Assess this cell for malaria.
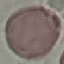
It is uninfected.

{
  "stain": "Giemsa",
  "image_type": "automatically extracted cell patch, resized to 64 × 64 pixels",
  "preparation": "thin blood smear",
  "capture": "smartphone camera at the microscope eyepiece"
}